Assess this cell for malaria.
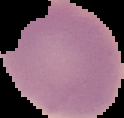
It is uninfected.

{
  "preparation": "thin blood film",
  "image_type": "cell region segmented out of the field of view; surrounding area masked to black",
  "image_size": "124×118 pixels"
}